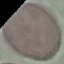

Summary:
  - Malaria status: uninfected
  - Capture: smartphone camera at the microscope eyepiece
  - Stain: Giemsa
  - Preparation: thin blood smear
  - Image type: cell patch, automatically extracted from a larger field of view and resized to 64 × 64 pixels